Assess the morphology of the red blood cells.
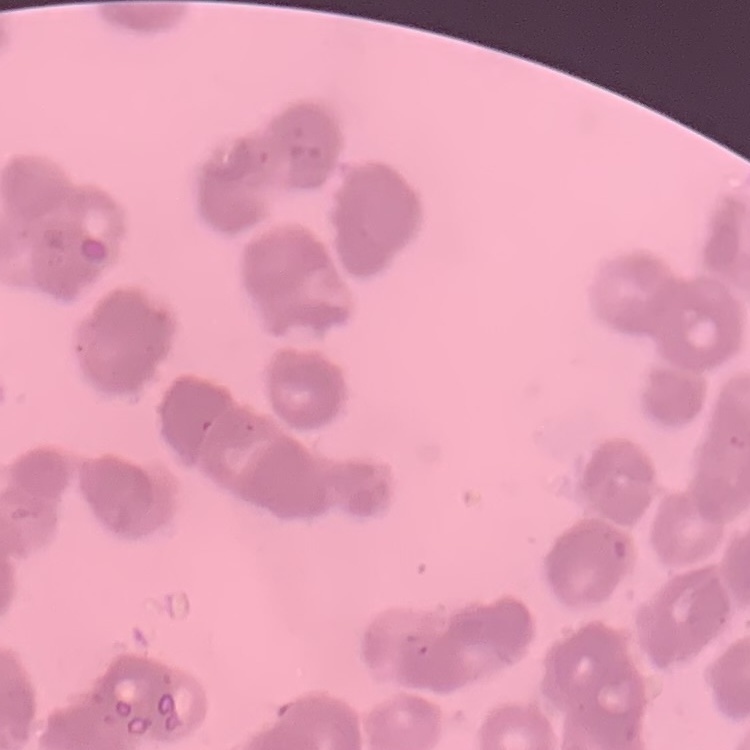
Rouleaux formation.

Thin blood film. Square crop of a larger photomicrograph. Field's or Giemsa stain.